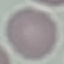
result = no malaria parasites detected
preparation = thin blood film
stain = Giemsa
image type = cell patch, automatically extracted from a larger field of view and resized to 64 × 64 pixels
capture = smartphone camera at the microscope eyepiece